Locate every uninfected red blood cell.
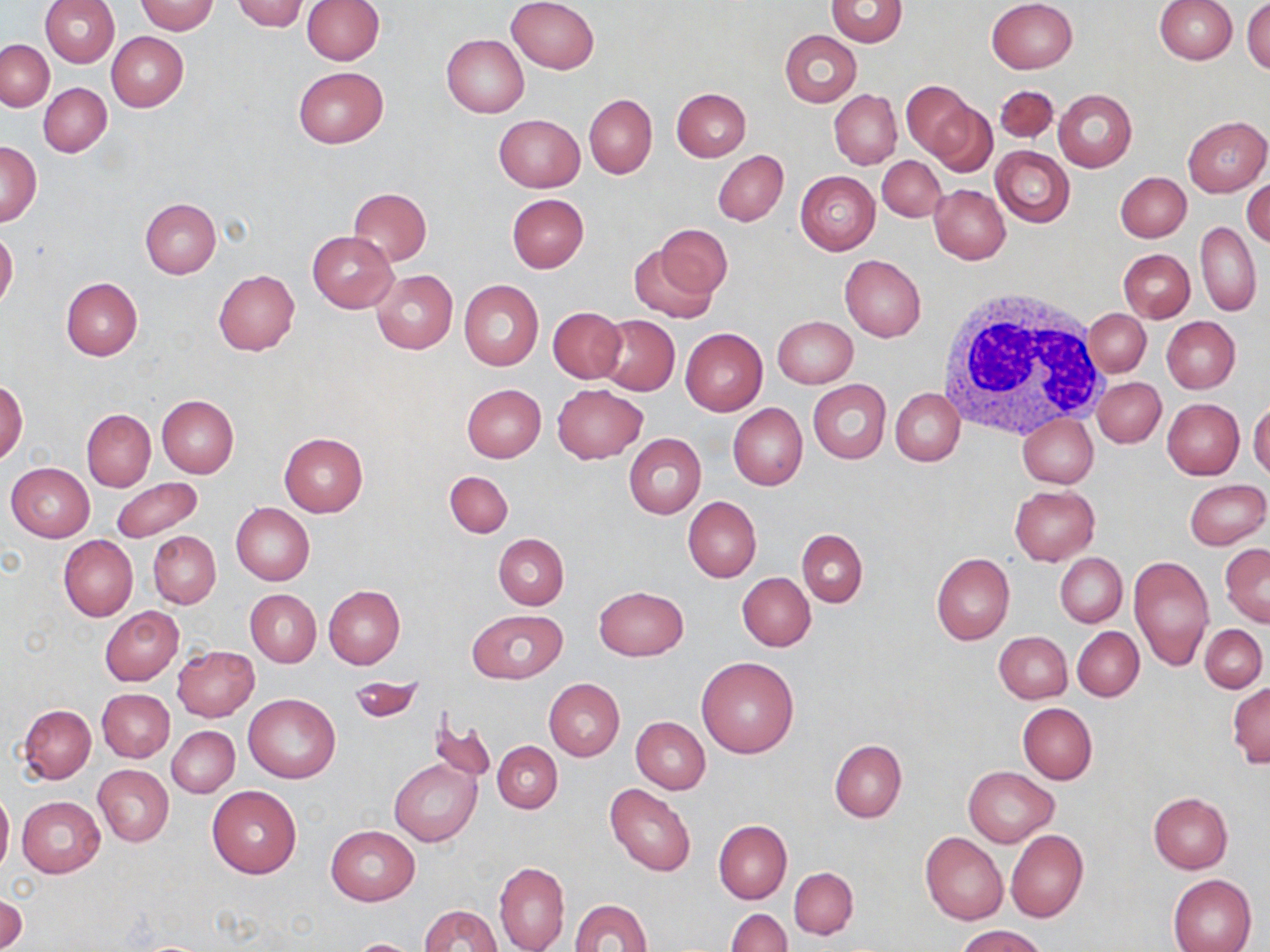
Approximate bounding boxes as [x1, y1, x2, y2] in pixels.
Uninfected red blood cells: [231, 0, 309, 31], [302, 0, 384, 65], [505, 0, 599, 74], [987, 0, 1077, 73], [1154, 0, 1237, 63], [1243, 0, 1270, 73], [40, 1, 119, 67], [134, 1, 218, 34], [825, 1, 908, 47], [780, 30, 861, 107], [106, 31, 188, 111], [441, 34, 529, 117], [1, 39, 54, 111], [293, 66, 388, 148], [900, 82, 977, 164], [39, 83, 111, 157], [995, 84, 1059, 143], [672, 87, 750, 161], [1053, 89, 1137, 171], [830, 90, 902, 170], [585, 95, 657, 177], [924, 99, 996, 176], [494, 114, 586, 192], [1183, 116, 1270, 196], [1, 142, 40, 225], [992, 146, 1075, 228], [713, 150, 788, 226], [877, 156, 946, 222], [795, 171, 879, 255], [1116, 171, 1190, 243], [1244, 178, 1270, 248], [930, 184, 1010, 263], [348, 187, 432, 265], [507, 194, 589, 273], [140, 198, 221, 279], [1196, 221, 1261, 316], [654, 224, 733, 299], [0, 229, 18, 309], [308, 231, 396, 313], [627, 243, 720, 323], [1119, 248, 1194, 321], [840, 254, 926, 341], [213, 270, 300, 355], [371, 270, 457, 354], [61, 278, 142, 361], [459, 279, 544, 371], [547, 307, 626, 383], [1082, 308, 1150, 378], [596, 314, 679, 396], [772, 316, 857, 388], [1163, 316, 1240, 393], [680, 328, 767, 415], [1094, 376, 1165, 447], [808, 379, 891, 464], [1, 380, 28, 464], [462, 384, 545, 462], [553, 384, 646, 464], [891, 387, 965, 465], [156, 394, 239, 478], [1162, 399, 1244, 479], [1249, 399, 1270, 482], [728, 403, 807, 491], [82, 408, 155, 492], [1018, 412, 1097, 487], [278, 432, 367, 517], [624, 433, 706, 518], [6, 462, 95, 542], [444, 470, 514, 537], [111, 477, 204, 542], [1184, 479, 1269, 550], [1008, 486, 1099, 566], [683, 496, 761, 583], [231, 503, 314, 586], [797, 529, 868, 607], [149, 530, 220, 608], [494, 533, 568, 610], [59, 535, 138, 621], [1219, 543, 1270, 626], [931, 553, 1014, 645], [1056, 553, 1126, 627], [1128, 556, 1214, 669], [737, 573, 815, 651], [595, 585, 688, 661], [323, 586, 405, 668], [245, 590, 321, 667], [99, 607, 183, 685], [467, 609, 567, 684], [1199, 624, 1267, 693], [1073, 627, 1143, 701], [994, 630, 1072, 702], [172, 645, 259, 722], [696, 656, 800, 758], [347, 676, 424, 724], [544, 678, 624, 760], [1227, 681, 1269, 768], [97, 689, 173, 763], [244, 692, 340, 783], [1018, 703, 1098, 784], [18, 704, 96, 783], [428, 714, 496, 787], [631, 717, 710, 794], [167, 726, 239, 797], [830, 739, 907, 822], [493, 740, 563, 814], [389, 757, 481, 846], [94, 765, 174, 846], [964, 766, 1059, 847], [605, 784, 696, 877], [207, 785, 301, 878], [0, 787, 13, 875], [1149, 793, 1233, 874], [16, 797, 105, 878], [713, 820, 792, 903], [326, 825, 420, 905], [1005, 829, 1088, 923], [920, 832, 1007, 924], [494, 861, 570, 952], [790, 867, 857, 939], [1168, 874, 1257, 952], [1, 893, 26, 951], [569, 898, 651, 951], [418, 904, 505, 952], [725, 909, 792, 952], [958, 925, 1047, 952], [343, 938, 424, 951].

White blood cell locations: [938, 288, 1109, 441]. Slide-level diagnosis: negative for blood parasites. Single field of view. Optical microscopy. May-Grünwald-Giemsa-stained preparation. 1000x magnification. Thin blood film. Image is 1270×952 pixels.